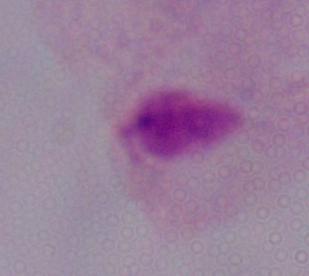

magnification = 1000x
modality = micrograph
identification = trichomonad